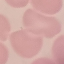
malaria status = uninfected
capture = smartphone camera at the microscope eyepiece
image type = automatically extracted cell patch, resized to 64 × 64 pixels
preparation = thin blood film
stain = Giemsa